Describe the morphology of the red blood cells.
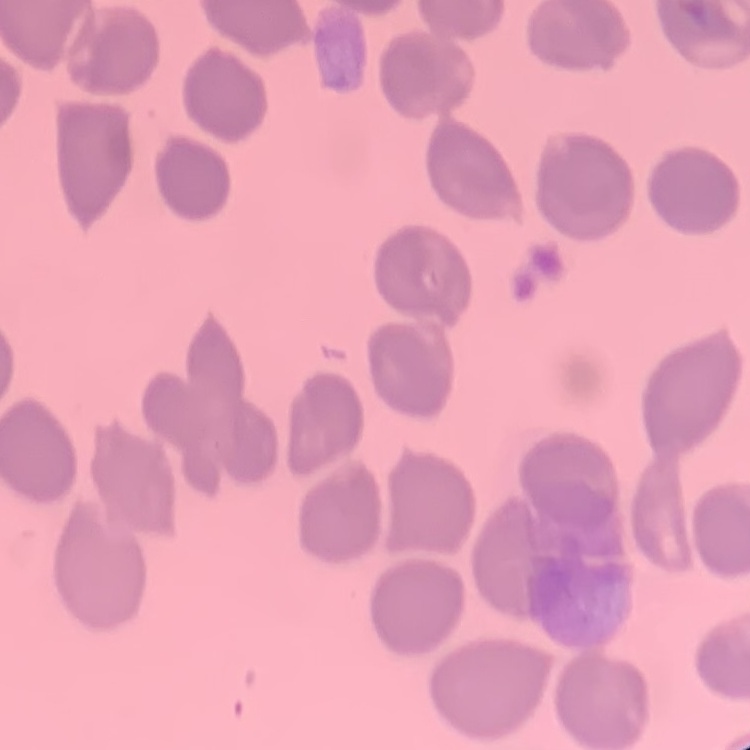

No rouleaux formation.

Thin blood film. Stained with either Field's or Giemsa. One tile cut from a larger photomicrograph.